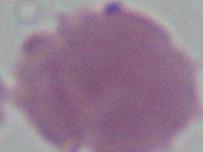
Summary:
  - Identification: erythrocyte
  - Magnification: 1000x
  - Modality: photomicrograph